Assess this cell for malaria.
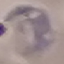
It is parasitized.

Photographed with a smartphone camera at the microscope eyepiece. Thin blood film. Automatically extracted cell patch, resized to 64 × 64 pixels. Giemsa-stained preparation.